Identify the blood parasite species.
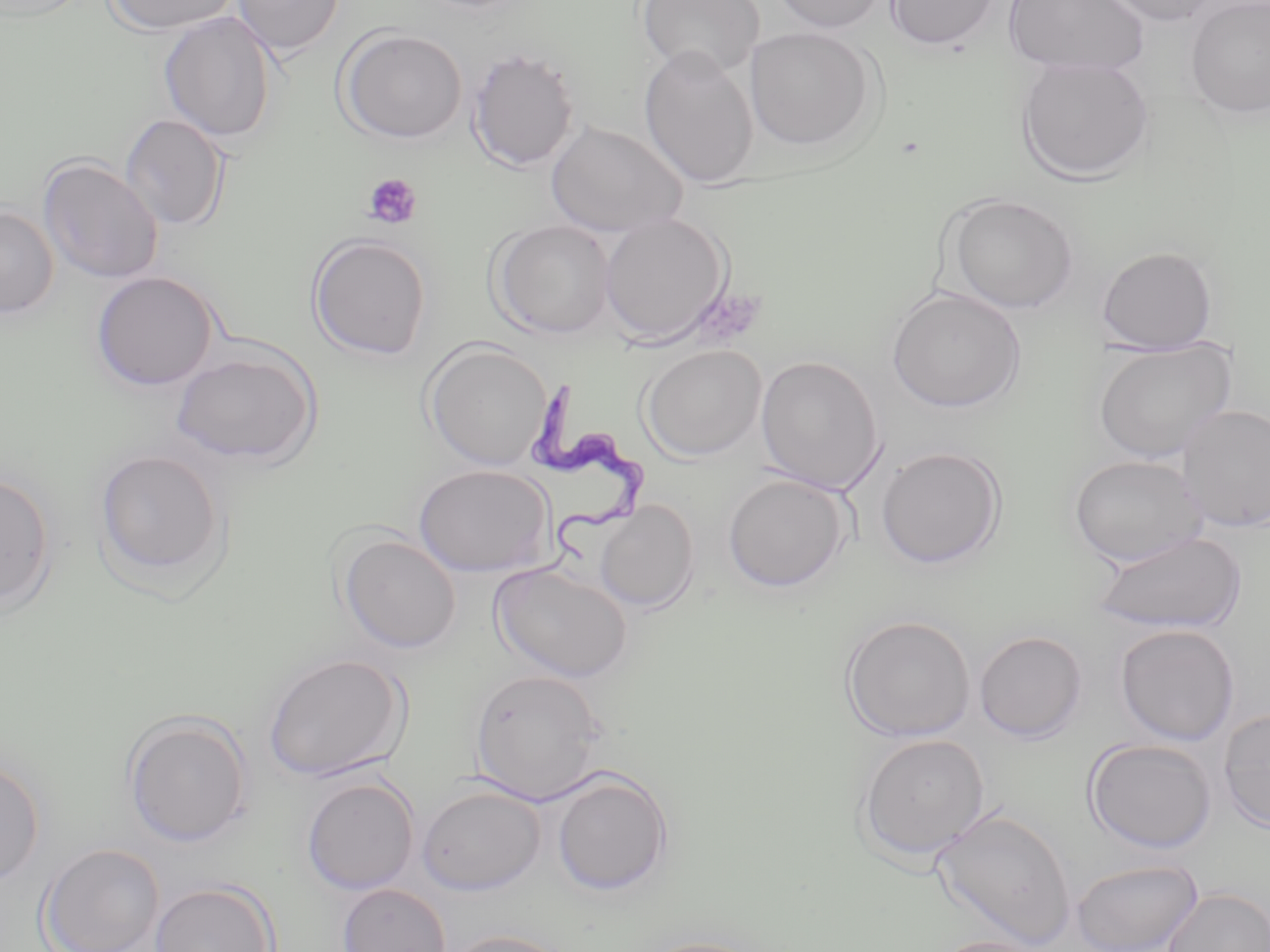

Trypanosoma brucei.

Summary:
  - Coordinate format: approximate bounding boxes as named x1/y1/x2/y2 corners in pixels
  - Trypanosoma brucei locations: (x1=529, y1=379, x2=650, y2=570)
  - Platelet locations: (x1=362, y1=172, x2=422, y2=229)
  - Uninfected red blood cell locations: (x1=103, y1=0, x2=241, y2=36), (x1=232, y1=0, x2=345, y2=58), (x1=636, y1=0, x2=765, y2=79), (x1=768, y1=0, x2=890, y2=35), (x1=884, y1=0, x2=1001, y2=51), (x1=1003, y1=0, x2=1149, y2=77), (x1=1101, y1=0, x2=1222, y2=26), (x1=1185, y1=0, x2=1270, y2=119), (x1=158, y1=10, x2=278, y2=143), (x1=336, y1=27, x2=467, y2=145), (x1=745, y1=27, x2=876, y2=151), (x1=638, y1=44, x2=760, y2=189), (x1=466, y1=47, x2=580, y2=173), (x1=1016, y1=55, x2=1155, y2=183), (x1=120, y1=113, x2=230, y2=232), (x1=546, y1=120, x2=688, y2=238), (x1=37, y1=155, x2=163, y2=284), (x1=943, y1=192, x2=1079, y2=314), (x1=0, y1=205, x2=59, y2=319), (x1=600, y1=212, x2=731, y2=346), (x1=490, y1=220, x2=616, y2=339), (x1=307, y1=233, x2=432, y2=361), (x1=1096, y1=245, x2=1219, y2=355), (x1=90, y1=271, x2=220, y2=391), (x1=887, y1=287, x2=1026, y2=413), (x1=1092, y1=338, x2=1237, y2=464), (x1=423, y1=342, x2=553, y2=470), (x1=170, y1=345, x2=322, y2=468), (x1=640, y1=345, x2=767, y2=462), (x1=755, y1=355, x2=885, y2=495), (x1=1177, y1=404, x2=1270, y2=533), (x1=875, y1=446, x2=1007, y2=569), (x1=93, y1=448, x2=229, y2=586), (x1=1067, y1=455, x2=1209, y2=567), (x1=413, y1=464, x2=554, y2=577), (x1=0, y1=471, x2=57, y2=614), (x1=722, y1=473, x2=852, y2=593), (x1=595, y1=501, x2=700, y2=613), (x1=1091, y1=530, x2=1248, y2=635), (x1=337, y1=532, x2=462, y2=654), (x1=490, y1=562, x2=634, y2=683), (x1=839, y1=615, x2=977, y2=742), (x1=1114, y1=624, x2=1240, y2=746), (x1=973, y1=630, x2=1088, y2=743), (x1=261, y1=652, x2=411, y2=783), (x1=469, y1=668, x2=610, y2=805), (x1=1217, y1=707, x2=1270, y2=833), (x1=121, y1=710, x2=254, y2=847), (x1=854, y1=733, x2=991, y2=864), (x1=1083, y1=738, x2=1218, y2=854), (x1=0, y1=758, x2=46, y2=886), (x1=550, y1=767, x2=674, y2=897), (x1=300, y1=776, x2=420, y2=895), (x1=416, y1=783, x2=547, y2=895), (x1=931, y1=806, x2=1077, y2=950), (x1=38, y1=843, x2=165, y2=952), (x1=1071, y1=858, x2=1203, y2=952), (x1=149, y1=880, x2=279, y2=952), (x1=337, y1=883, x2=451, y2=952), (x1=1162, y1=887, x2=1270, y2=952), (x1=443, y1=928, x2=577, y2=952), (x1=632, y1=935, x2=768, y2=952), (x1=929, y1=935, x2=1054, y2=952)
  - Image size: 1270×952 pixels
  - Stain: May-Grünwald-Giemsa
  - Field of view: single
  - Modality: light microscopy
  - Magnification: 1000x
  - Preparation: thin blood smear